Point out malaria parasites and leukocytes.
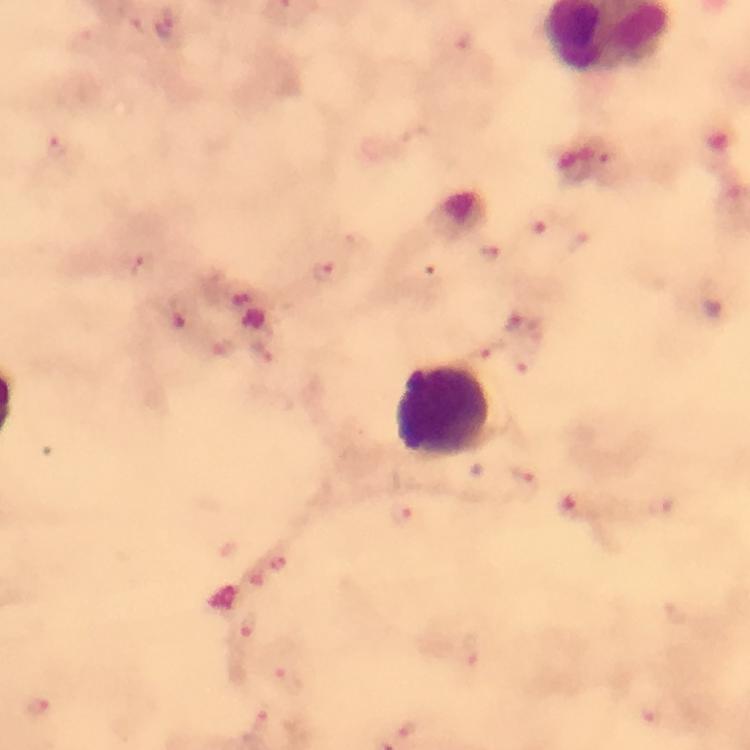
Approximate centers as {x, y} in pixels.
Malaria parasites: {163, 25}, {57, 148}, {539, 219}, {576, 241}, {491, 253}, {142, 265}, {326, 272}, {180, 311}, {484, 345}, {263, 352}, {524, 363}, {525, 488}, {407, 517}, {247, 625}, {472, 649}, {285, 677}, {38, 707}, {408, 726}, {254, 727}.
Leukocytes: {443, 410}.

Summary:
  - Cropped from: a single field of view
  - Context: from a diagnostic examination for malaria
  - Preparation: thick blood film
  - Image size: 750×750 pixels
  - Immersion oil: used
  - Stain: Giemsa
  - Capture: smartphone photograph through a microscope
  - Magnification: 100x